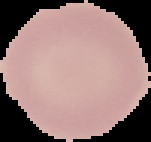
image_type: cell region segmented out of the field of view; surrounding area masked to black
malaria_status: uninfected
image_size: 151×142 pixels
preparation: thin blood film